Outline each Plasmodium falciparum-infected red blood cell.
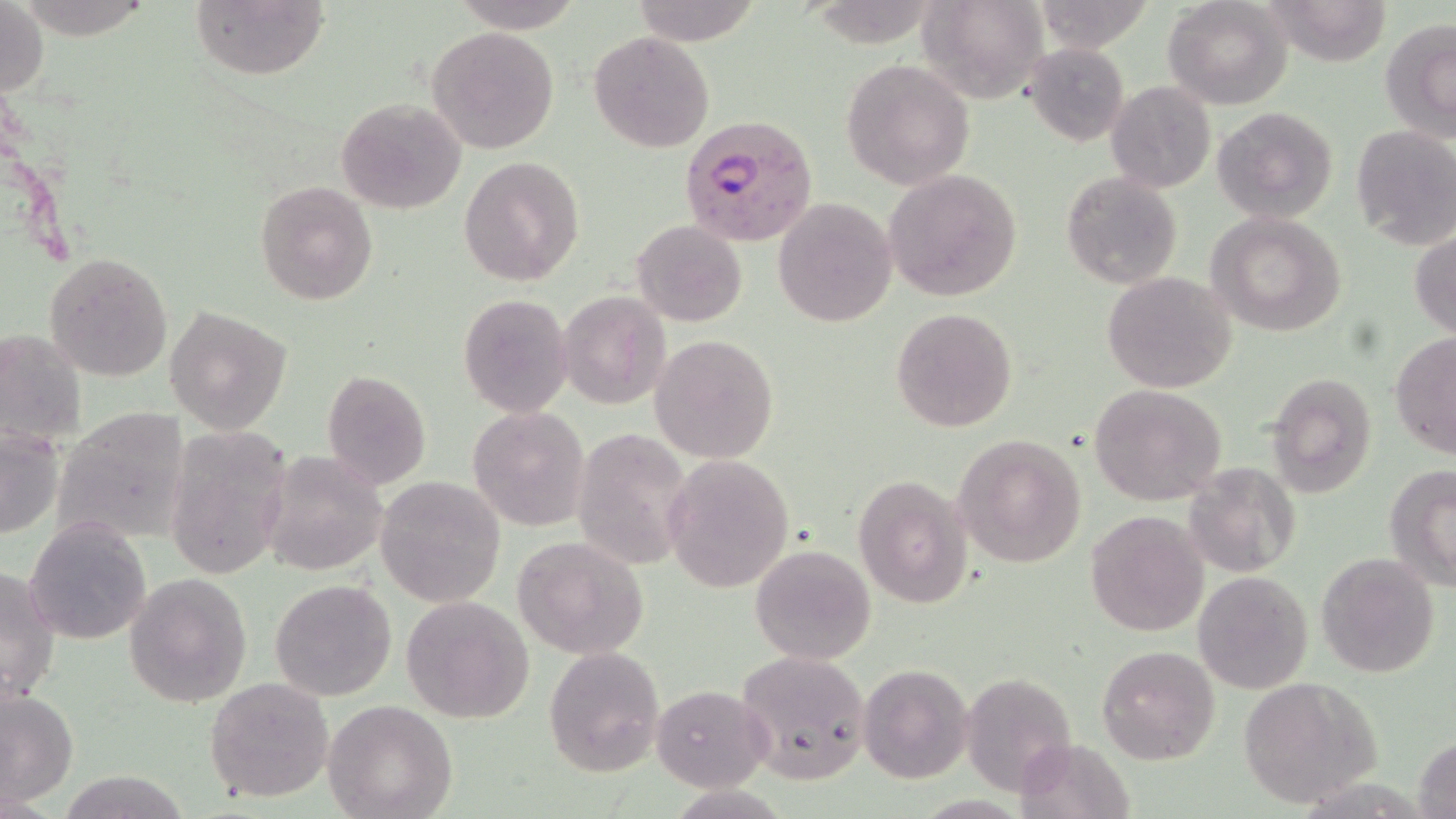
Approximate bounding boxes as [x1, y1, x2, y2] in pixels.
Plasmodium falciparum-infected red blood cells: [682, 118, 817, 246].

Summary:
  - Uninfected red blood cell locations: [629, 0, 765, 46], [917, 0, 1048, 103], [1163, 0, 1293, 110], [1263, 0, 1394, 65], [190, 1, 329, 81], [452, 1, 584, 33], [0, 2, 49, 100], [1380, 18, 1456, 142], [427, 25, 560, 154], [589, 31, 713, 153], [1026, 44, 1131, 145], [841, 58, 975, 191], [1105, 81, 1216, 194], [334, 96, 467, 215], [1212, 105, 1340, 225], [1349, 124, 1456, 249], [459, 156, 584, 286], [883, 169, 1024, 301], [1061, 172, 1182, 289], [255, 180, 379, 304], [773, 197, 899, 327], [1206, 212, 1348, 336], [631, 220, 747, 328], [1410, 230, 1456, 340], [43, 252, 175, 381], [1102, 271, 1240, 393], [558, 291, 670, 408], [457, 292, 574, 419], [165, 305, 291, 433], [890, 306, 1018, 432], [0, 327, 87, 445], [1390, 333, 1456, 459], [651, 334, 780, 464], [320, 369, 432, 490], [1267, 370, 1378, 497], [1088, 383, 1226, 505], [469, 406, 591, 531], [53, 407, 192, 549], [0, 424, 63, 539], [573, 426, 692, 569], [164, 428, 293, 581], [954, 434, 1088, 567], [262, 451, 387, 576], [664, 455, 795, 595], [1184, 461, 1303, 577], [1385, 463, 1456, 588], [854, 473, 974, 608], [375, 475, 506, 608], [1084, 511, 1209, 637], [26, 518, 150, 645], [513, 534, 649, 660], [750, 544, 875, 665], [1315, 553, 1440, 677], [0, 565, 61, 704], [124, 571, 253, 707], [1194, 571, 1312, 693], [269, 579, 397, 702], [399, 596, 534, 722], [545, 645, 665, 776], [1097, 646, 1220, 765], [735, 649, 873, 783], [858, 663, 973, 783], [960, 671, 1077, 797], [205, 677, 334, 802], [1238, 677, 1382, 809], [650, 685, 770, 791], [0, 688, 79, 805], [323, 699, 457, 819], [1414, 733, 1456, 819], [59, 772, 189, 817]
  - Slide-level diagnosis: Plasmodium falciparum
  - Image size: 1456×819 pixels
  - Stain: May-Grünwald-Giemsa
  - Field of view: single
  - Modality: light microscopy
  - Magnification: 1000x
  - Preparation: thin blood smear